Identify the parasite.
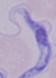
This is a trypanosome.

Summary:
  - Magnification: 1000x
  - Modality: micrograph